Report the malaria status of this cell.
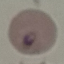

Parasitized.

{
  "preparation": "thin smear",
  "image_type": "automatically extracted cell patch, resized to 64 × 64 pixels",
  "stain": "Giemsa",
  "capture": "smartphone camera at the microscope eyepiece"
}